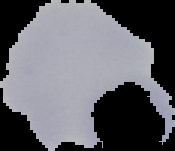
{
  "image_type": "segmented cell region with the area outside set to black",
  "malaria_status": "uninfected",
  "image_size": "175×151 pixels",
  "preparation": "thin blood film"
}